Assess for Plasmodium parasites.
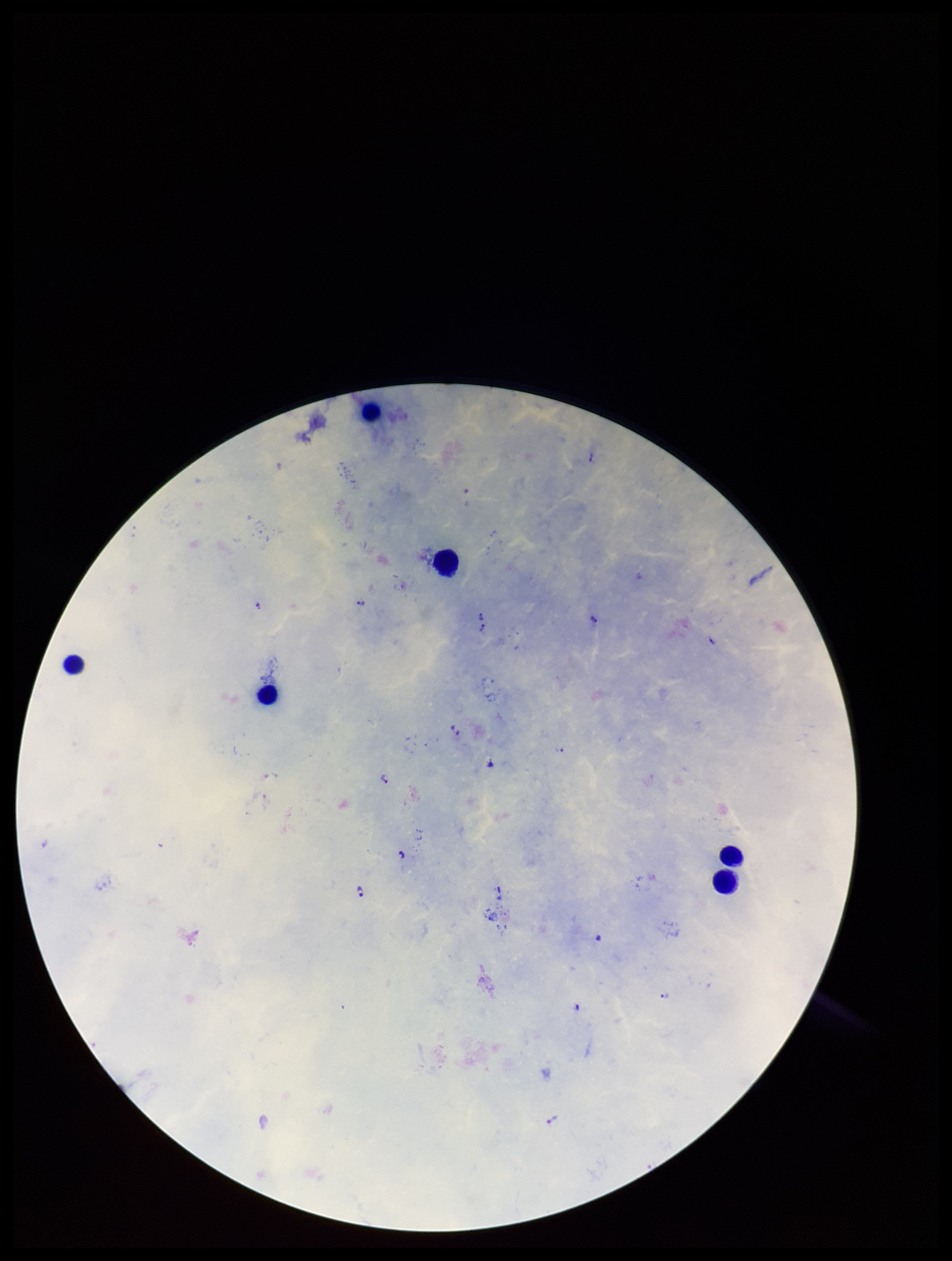

Identified.

Summary:
  - Species reported for this patient: Plasmodium falciparum
  - Parasite count: 15
  - Image size: 952×1261 pixels
  - Stain: Giemsa
  - Preparation: thick
  - Capture: smartphone photograph through the microscope eyepiece
  - Field of view: one from this slide
  - Leukocyte count: 6
  - Patient malaria status: infected